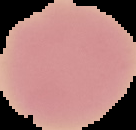 Result: no malaria parasites seen. The area outside the segmented cell region is set to black. Image is 136×130 pixels. From a thin blood film.